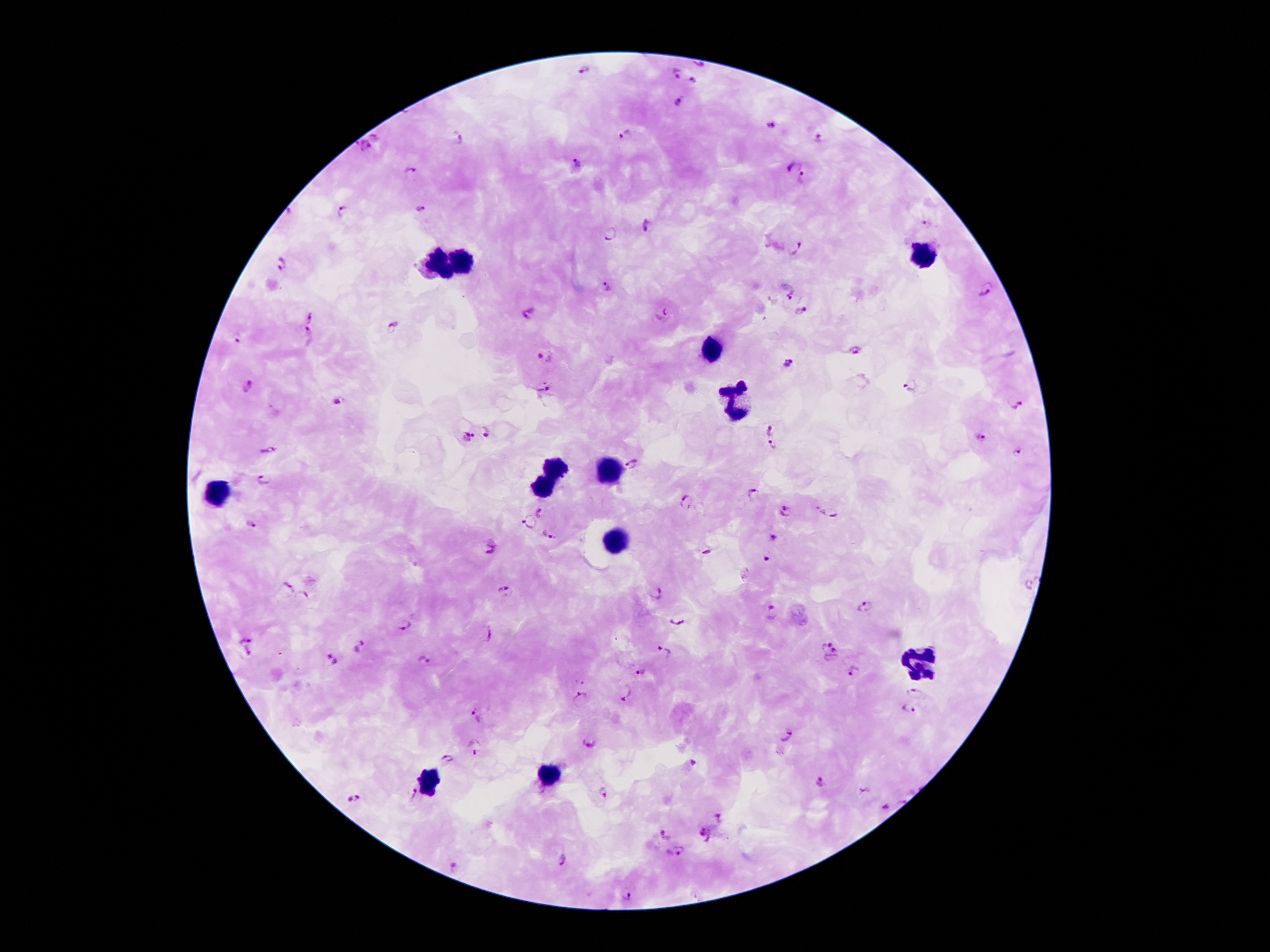
{
  "stain": "Giemsa",
  "preparation": "thick blood film",
  "capture": "smartphone camera through the microscope eyepiece",
  "image_size": "1270×952 pixels",
  "leukocyte_locations": "approximate centers as [x, y] in pixels: [923, 253], [463, 260], [436, 265], [711, 350], [734, 402], [556, 466], [608, 470], [543, 486], [218, 490], [617, 538], [919, 665], [547, 775], [428, 782]",
  "plasmodium_parasite_locations": "approximate centers as [x, y] in pixels: [586, 69], [675, 73], [693, 80], [677, 103], [771, 125], [626, 134], [377, 135], [460, 139], [818, 139], [364, 147], [578, 163], [793, 165], [409, 170], [802, 176], [419, 210], [341, 212], [927, 224], [647, 225], [609, 234], [795, 248], [282, 265], [608, 286], [987, 289], [785, 290], [802, 310], [531, 314], [662, 314], [310, 318], [391, 324], [235, 337], [308, 337], [855, 351], [543, 357], [788, 364], [248, 385], [543, 389], [910, 389], [339, 401], [1017, 404], [769, 430], [485, 431], [466, 434], [981, 437], [769, 445], [265, 451], [1017, 451], [633, 465], [264, 478], [751, 494], [687, 505], [784, 511], [830, 511], [542, 512], [251, 522], [528, 522], [550, 533], [776, 537], [492, 547], [766, 561], [286, 587], [504, 590], [658, 592], [303, 598], [863, 608], [773, 614], [678, 618], [407, 624], [488, 635], [245, 640], [360, 646], [824, 646], [665, 651], [248, 652], [834, 657], [420, 658], [332, 660], [642, 670], [852, 671], [626, 690], [914, 693], [581, 697], [910, 710], [476, 715], [787, 733], [588, 740], [476, 747], [448, 757], [819, 782], [600, 793], [412, 794], [352, 799], [886, 806], [721, 816], [704, 828], [665, 834], [677, 853], [560, 858], [453, 867], [628, 894]",
  "magnification": "100x",
  "field_of_view": "one from this slide",
  "patient_malaria_status": "infected with Plasmodium falciparum"
}